Describe the morphology of the erythrocytes.
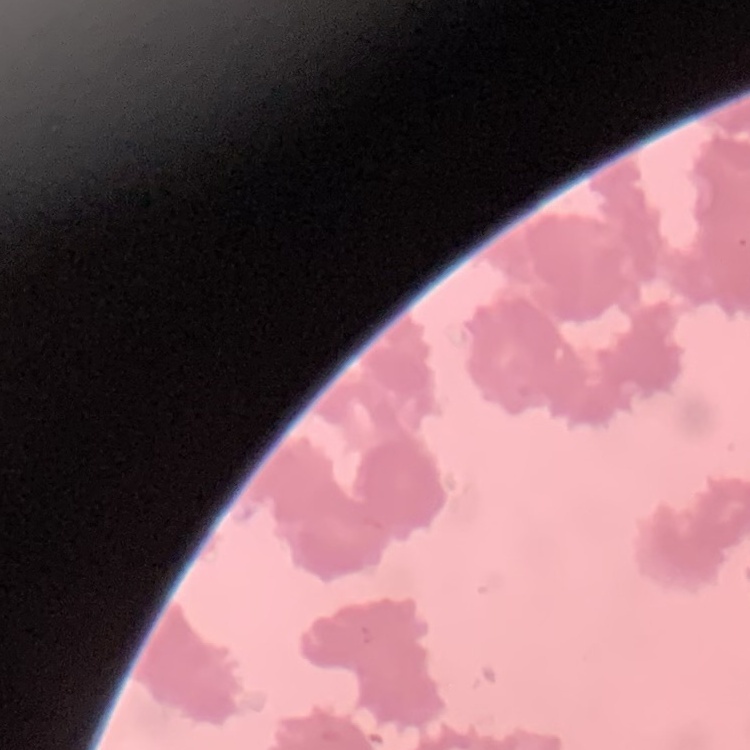

Rouleaux formation.

Summary:
  - Preparation: thin blood film
  - Image type: square crop of a larger photomicrograph
  - Stain: Field's or Giemsa